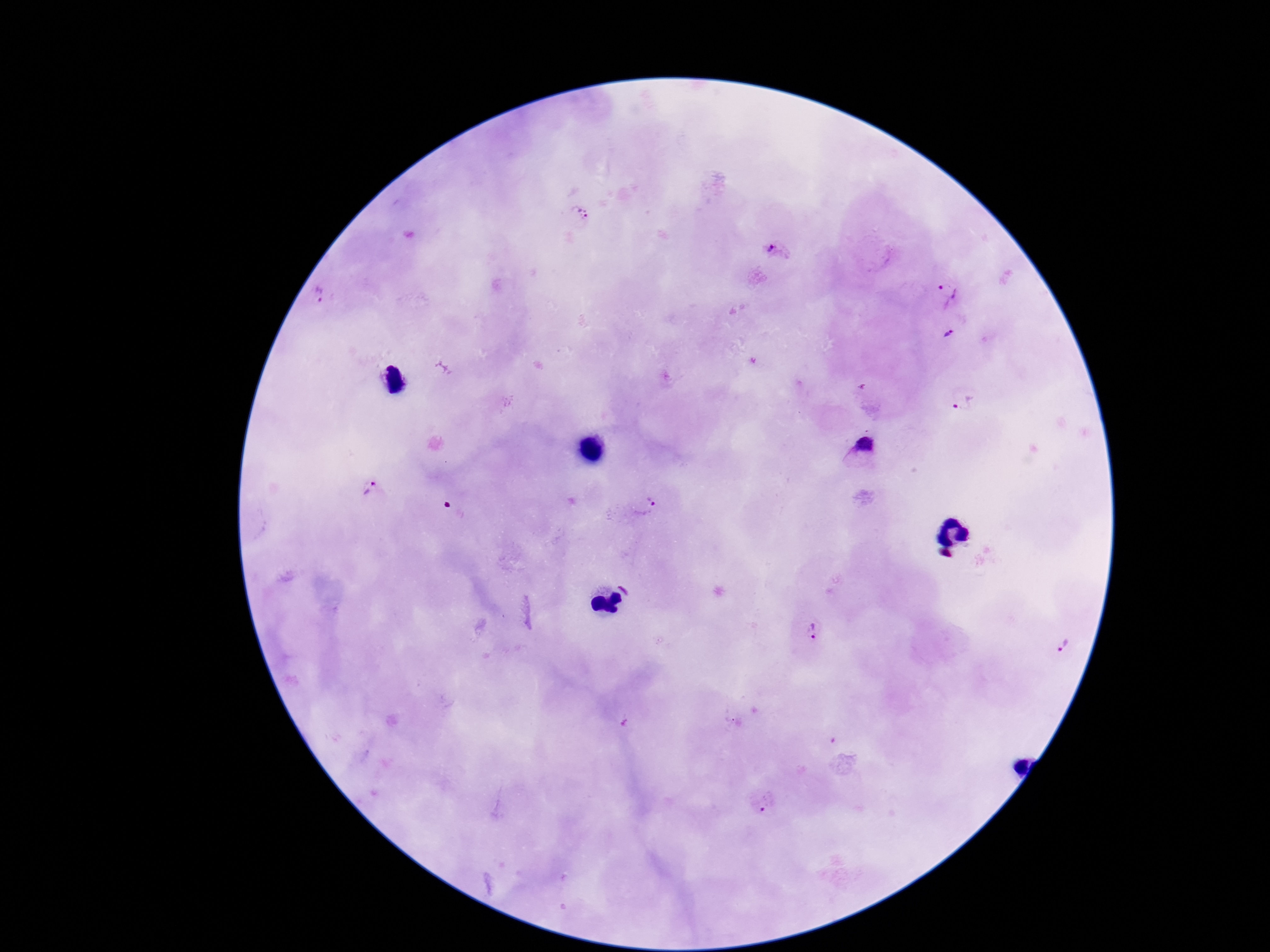

image size = 1270×952 pixels
Plasmodium parasite locations = approximate centers as [x, y] in pixels: [581, 216], [774, 251], [948, 290], [321, 298], [950, 334], [964, 403], [865, 446], [371, 491], [653, 499], [812, 633], [1065, 644], [766, 808]
preparation = thick blood smear
stain = Giemsa
capture = smartphone camera through the microscope eyepiece
patient malaria status = infected
field of view = one from this slide
magnification = 100x